Classify this cell by malaria status.
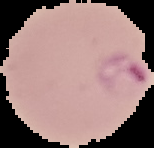

It is parasitized.

Cell region segmented out of the field of view; the surrounding area is masked to black. Image is 154×148 pixels. From a thin blood film.